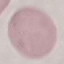
Malaria status: uninfected. Giemsa-stained preparation. Automatically extracted cell patch, resized to 64 × 64 pixels. Thin blood film. Photographed with a smartphone camera at the microscope eyepiece.